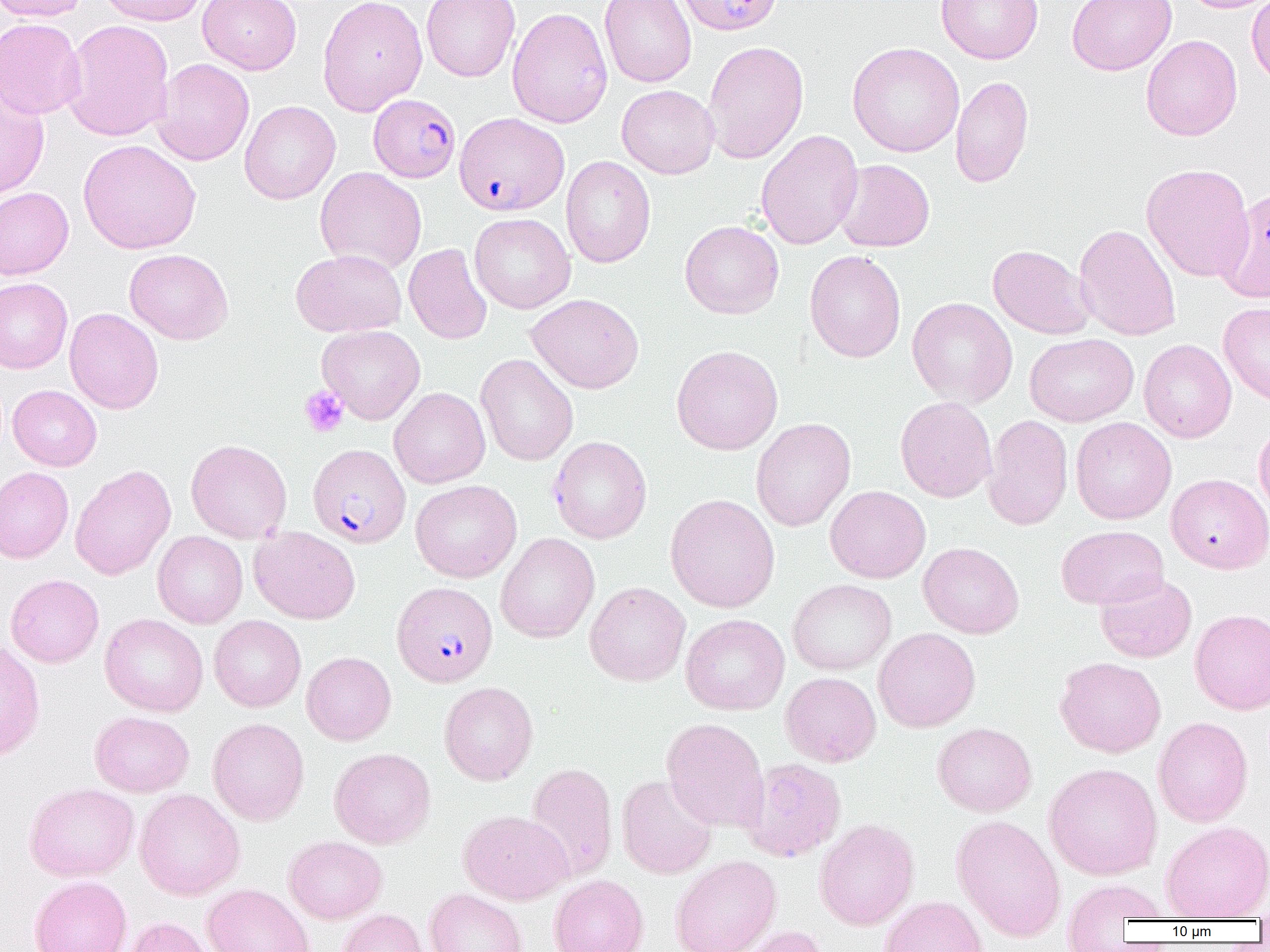

Plasmodium falciparum-infected red blood cell locations = approximate bounding boxes as [x1, y1, x2, y2] in pixels: [677, 0, 783, 35], [368, 94, 460, 182], [454, 112, 569, 215], [308, 443, 411, 549], [392, 581, 498, 687]
slide-level diagnosis = Plasmodium falciparum
field of view = single
image size = 1270×952 pixels
magnification = 1000x
platelet locations = approximate bounding boxes as [x1, y1, x2, y2] in pixels: [300, 386, 349, 438]
modality = optical microscopy
uninfected red blood cell locations = approximate bounding boxes as [x1, y1, x2, y2] in pixels: [0, 0, 90, 21], [97, 0, 208, 26], [198, 0, 301, 74], [318, 0, 428, 116], [421, 0, 521, 82], [599, 0, 697, 88], [936, 0, 1043, 64], [1067, 0, 1177, 76], [1181, 0, 1270, 13], [1247, 0, 1270, 88], [507, 6, 613, 128], [0, 17, 86, 120], [62, 19, 174, 142], [1141, 34, 1242, 141], [702, 40, 809, 164], [847, 42, 965, 157], [151, 58, 255, 166], [950, 75, 1034, 188], [0, 84, 49, 199], [617, 84, 720, 179], [239, 101, 341, 204], [755, 130, 864, 250], [78, 139, 201, 254], [561, 156, 656, 268], [834, 159, 935, 252], [1141, 163, 1253, 282], [315, 167, 427, 274], [0, 187, 74, 279], [1217, 188, 1270, 303], [469, 213, 576, 313], [680, 220, 784, 319], [1074, 224, 1181, 341], [404, 243, 492, 345], [987, 244, 1096, 339], [124, 249, 233, 345], [290, 249, 406, 337], [804, 250, 906, 363], [0, 278, 73, 374], [526, 293, 644, 394], [907, 297, 1018, 408], [1219, 301, 1270, 407], [64, 308, 163, 414], [317, 325, 426, 425], [1025, 333, 1138, 427], [1138, 339, 1236, 442], [671, 345, 783, 455], [475, 354, 578, 466], [8, 385, 102, 471], [389, 387, 490, 488], [895, 396, 997, 503], [982, 414, 1073, 530], [1070, 417, 1177, 524], [751, 418, 855, 531], [1254, 421, 1270, 523], [548, 436, 652, 544], [186, 439, 292, 543], [70, 464, 176, 580], [0, 467, 74, 563], [1166, 473, 1270, 574], [410, 479, 522, 583], [825, 485, 931, 583], [665, 493, 780, 613], [1055, 525, 1168, 610], [249, 526, 360, 624], [153, 531, 248, 628], [496, 533, 599, 643], [918, 541, 1024, 638], [6, 573, 103, 667], [1095, 573, 1197, 663], [788, 579, 897, 675], [584, 581, 690, 686], [1190, 608, 1270, 714], [680, 613, 790, 715], [100, 614, 208, 716], [209, 615, 306, 712], [873, 628, 981, 733], [0, 640, 46, 763], [302, 651, 396, 745], [1055, 656, 1166, 758], [781, 672, 881, 767], [439, 681, 538, 785], [90, 711, 194, 797], [1153, 716, 1253, 827], [207, 718, 309, 825], [661, 718, 769, 833], [932, 722, 1037, 816], [329, 747, 435, 849], [741, 758, 847, 863], [526, 762, 617, 881], [1044, 762, 1162, 880], [617, 775, 718, 879], [24, 782, 139, 881], [135, 789, 245, 900], [458, 809, 573, 905], [951, 814, 1066, 942], [814, 819, 919, 930], [1160, 820, 1270, 921], [284, 835, 387, 924], [670, 855, 781, 952], [549, 874, 647, 952], [30, 875, 132, 952], [1060, 877, 1170, 943], [202, 883, 314, 952], [424, 888, 528, 952], [879, 895, 989, 952], [336, 908, 429, 952], [123, 916, 217, 952], [733, 925, 829, 952]
preparation = thin blood film